Name the parasite shown.
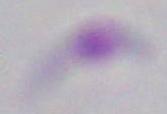
Toxoplasma gondii.

Photomicrograph. Captured at 1000x magnification.